Classify this cell by malaria status.
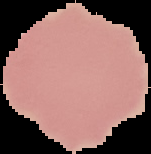

Uninfected.

From a thin blood smear. Image is 151×154 pixels. Segmented cell region on a black background.